Classify this cell by malaria status.
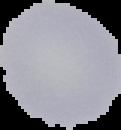

It is uninfected.

Summary:
  - Image size: 121×130 pixels
  - Image type: segmented cell region on a black background
  - Preparation: thin blood film